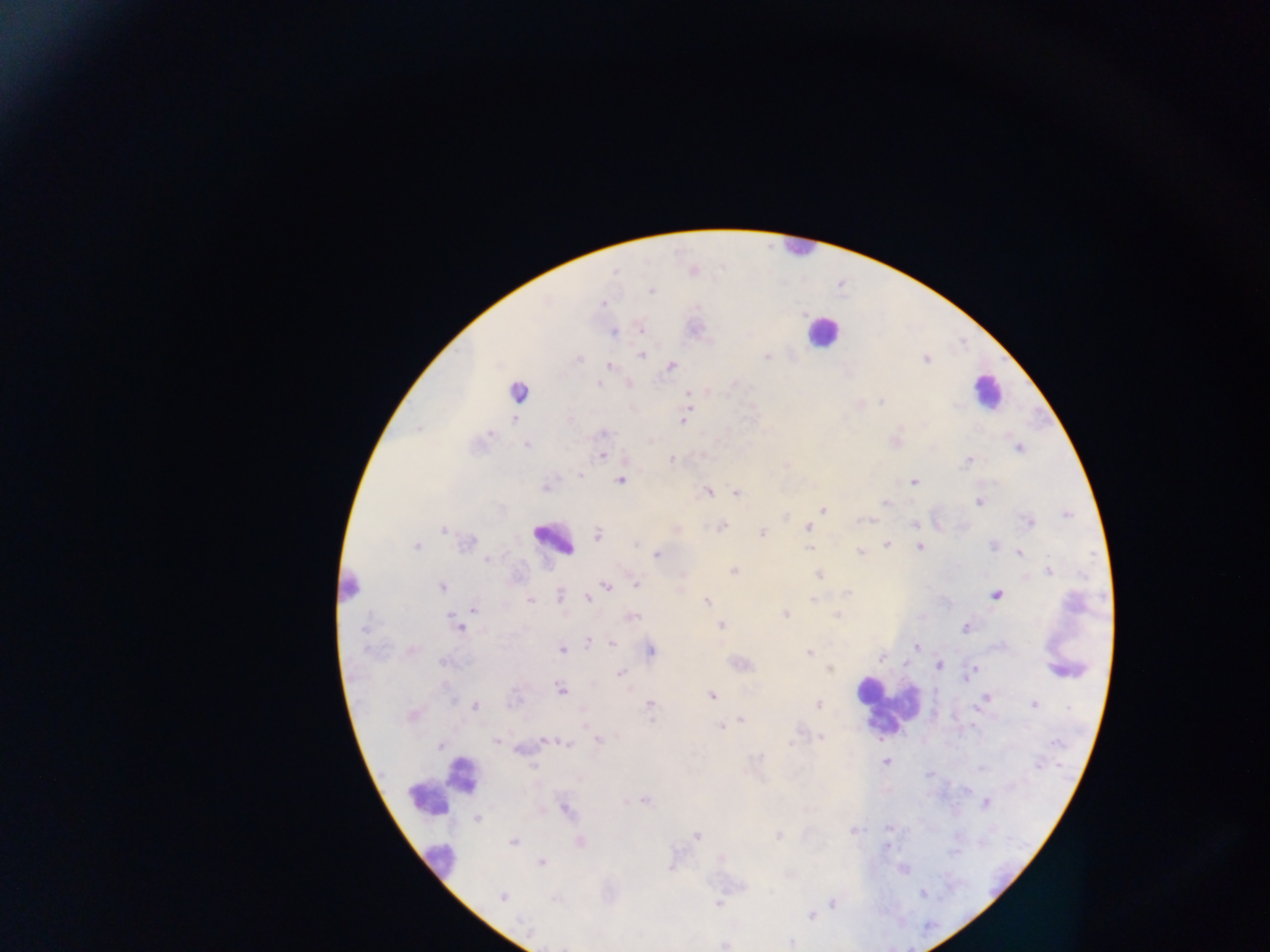 Approximate centers as (x, y) in pixels. Plasmodium parasite locations: (686, 393), (690, 409), (513, 419), (683, 420), (605, 434), (527, 445), (604, 456), (671, 460), (579, 473), (621, 481), (914, 483), (542, 487), (735, 493), (979, 502), (822, 510), (722, 526), (807, 528), (762, 533), (598, 535), (920, 546), (809, 549), (1020, 554), (655, 555), (734, 570), (819, 575), (636, 583), (443, 587), (606, 588), (994, 595), (590, 599), (530, 600), (707, 602), (474, 608), (449, 617), (720, 626), (965, 628), (461, 629), (611, 644), (916, 647), (562, 650), (652, 652), (881, 657), (940, 664), (621, 673), (560, 688), (711, 696), (742, 719), (720, 726), (885, 761). Leukocyte locations: (796, 248), (818, 336), (984, 395), (548, 539), (346, 588), (885, 712), (440, 787), (442, 867). Image is 1270×952 pixels. Sample from Ghana. Thick blood smear. One field of view. Mobile-phone photograph taken through the microscope.